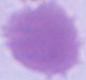
Summary:
  - Modality: micrograph
  - Magnification: 1000x
  - Identification: red blood cell